Report the malaria status of this cell.
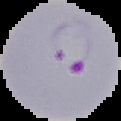
Parasitized.

From a thin blood film. Segmented cell region on a black background. Image is 121×121 pixels.